Assess the morphology of the erythrocytes.
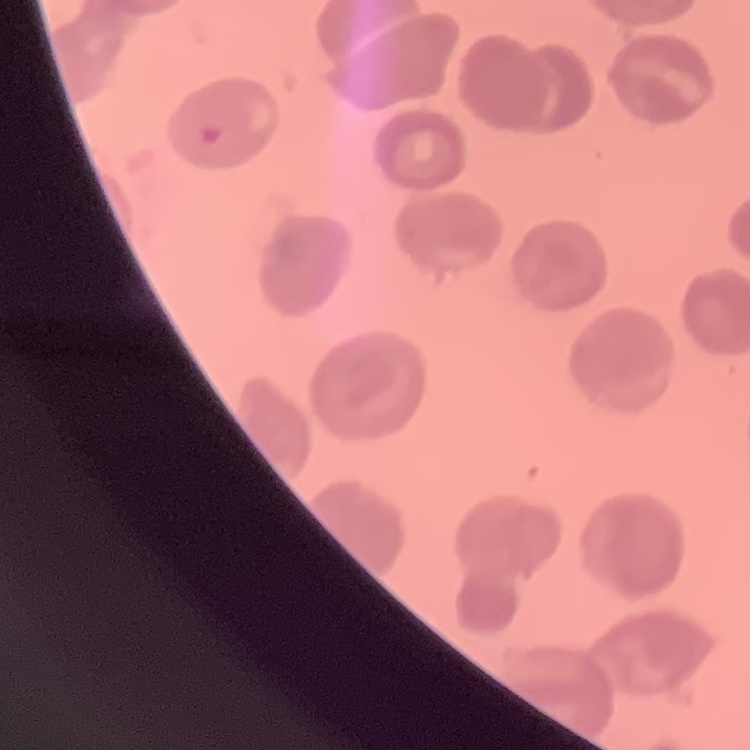
They show no rouleaux formation.

Square crop of a larger photomicrograph. Stained with either Field's or Giemsa. Thin blood film.